Mark where platelets are.
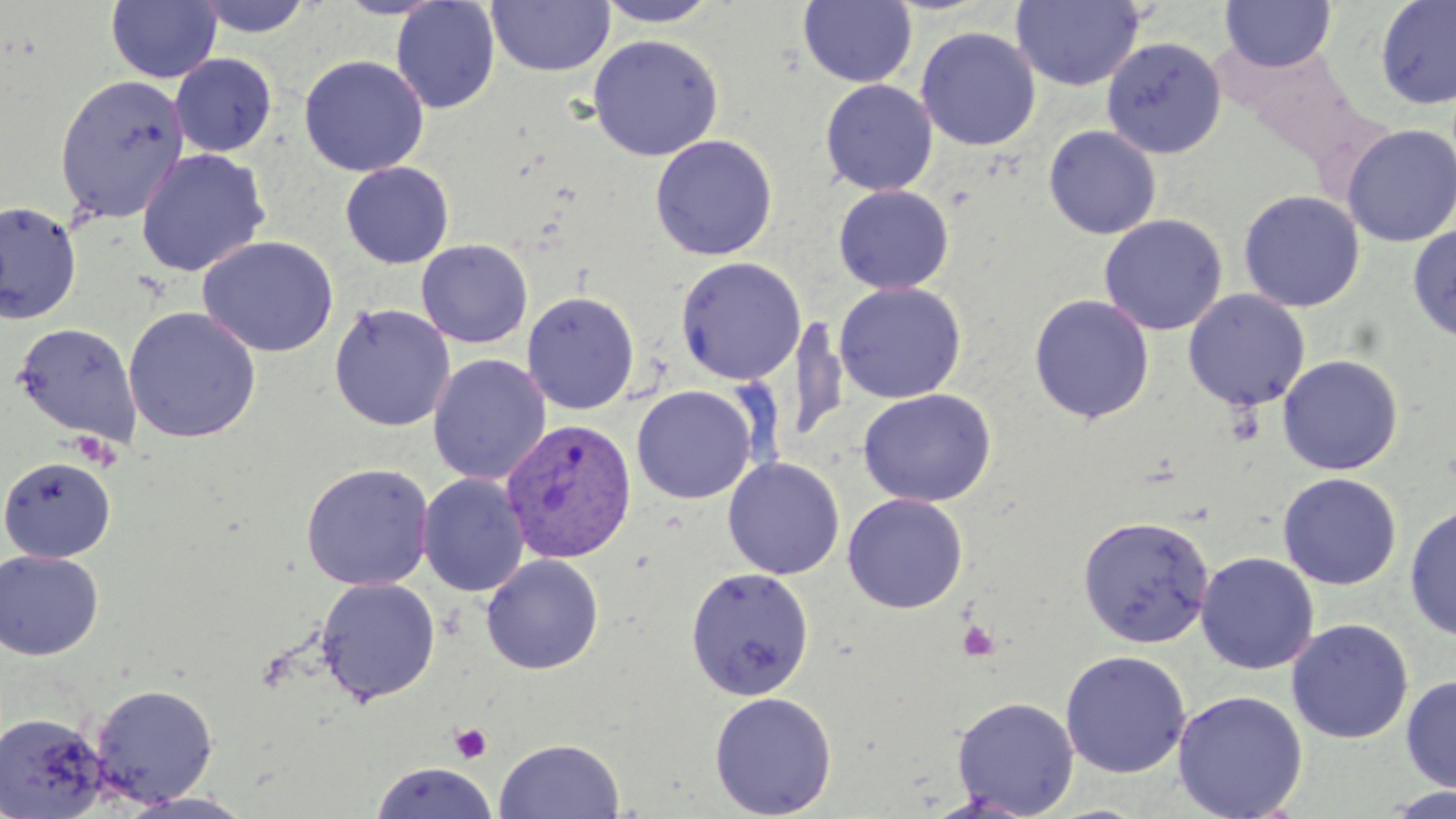
Approximate bounding boxes as named x1/y1/x2/y2 corners in pixels.
Platelets: (x1=957, y1=620, x2=1000, y2=661), (x1=450, y1=722, x2=492, y2=763).

Uninfected red blood cell locations: (x1=106, y1=0, x2=222, y2=84), (x1=191, y1=0, x2=316, y2=38), (x1=390, y1=0, x2=500, y2=114), (x1=592, y1=0, x2=724, y2=27), (x1=1011, y1=0, x2=1146, y2=92), (x1=1221, y1=0, x2=1337, y2=73), (x1=1375, y1=0, x2=1456, y2=110), (x1=486, y1=1, x2=615, y2=77), (x1=798, y1=1, x2=918, y2=88), (x1=916, y1=26, x2=1041, y2=151), (x1=587, y1=34, x2=724, y2=161), (x1=1101, y1=36, x2=1227, y2=159), (x1=169, y1=53, x2=277, y2=157), (x1=299, y1=55, x2=429, y2=177), (x1=54, y1=73, x2=190, y2=224), (x1=820, y1=79, x2=938, y2=196), (x1=1341, y1=124, x2=1456, y2=247), (x1=1043, y1=125, x2=1162, y2=239), (x1=650, y1=134, x2=778, y2=261), (x1=135, y1=148, x2=270, y2=277), (x1=340, y1=162, x2=454, y2=268), (x1=833, y1=184, x2=954, y2=294), (x1=1238, y1=190, x2=1365, y2=312), (x1=0, y1=200, x2=83, y2=325), (x1=1099, y1=214, x2=1227, y2=336), (x1=1407, y1=224, x2=1456, y2=344), (x1=198, y1=235, x2=338, y2=358), (x1=416, y1=239, x2=533, y2=348), (x1=675, y1=256, x2=806, y2=385), (x1=833, y1=282, x2=967, y2=403), (x1=1183, y1=290, x2=1310, y2=411), (x1=521, y1=291, x2=640, y2=415), (x1=1029, y1=294, x2=1154, y2=424), (x1=329, y1=303, x2=455, y2=432), (x1=123, y1=306, x2=262, y2=444), (x1=789, y1=314, x2=849, y2=446), (x1=13, y1=321, x2=142, y2=446), (x1=427, y1=353, x2=550, y2=486), (x1=1278, y1=354, x2=1404, y2=475), (x1=631, y1=384, x2=757, y2=504), (x1=857, y1=388, x2=997, y2=507), (x1=0, y1=456, x2=116, y2=563), (x1=722, y1=457, x2=845, y2=579), (x1=300, y1=462, x2=435, y2=591), (x1=1278, y1=472, x2=1402, y2=590), (x1=417, y1=473, x2=529, y2=597), (x1=843, y1=494, x2=968, y2=613), (x1=1404, y1=503, x2=1456, y2=642), (x1=1077, y1=514, x2=1214, y2=648), (x1=0, y1=549, x2=104, y2=660), (x1=1195, y1=552, x2=1319, y2=675), (x1=481, y1=554, x2=604, y2=675), (x1=685, y1=567, x2=815, y2=700), (x1=314, y1=576, x2=440, y2=705), (x1=1286, y1=619, x2=1413, y2=744), (x1=1060, y1=650, x2=1191, y2=778), (x1=1400, y1=674, x2=1456, y2=794), (x1=90, y1=683, x2=219, y2=806), (x1=1172, y1=690, x2=1308, y2=819), (x1=709, y1=691, x2=837, y2=819), (x1=951, y1=696, x2=1079, y2=817), (x1=0, y1=712, x2=107, y2=817), (x1=493, y1=737, x2=626, y2=819), (x1=371, y1=762, x2=496, y2=818), (x1=1381, y1=786, x2=1456, y2=819), (x1=118, y1=791, x2=259, y2=819). Plasmodium vivax-infected red blood cell locations: (x1=501, y1=419, x2=637, y2=563). Slide-level diagnosis: Plasmodium vivax. Light microscopy. Captured at 1000x magnification. Thin blood film. May-Grünwald-Giemsa-stained preparation. One field of a larger specimen. Image is 1456×819 pixels.